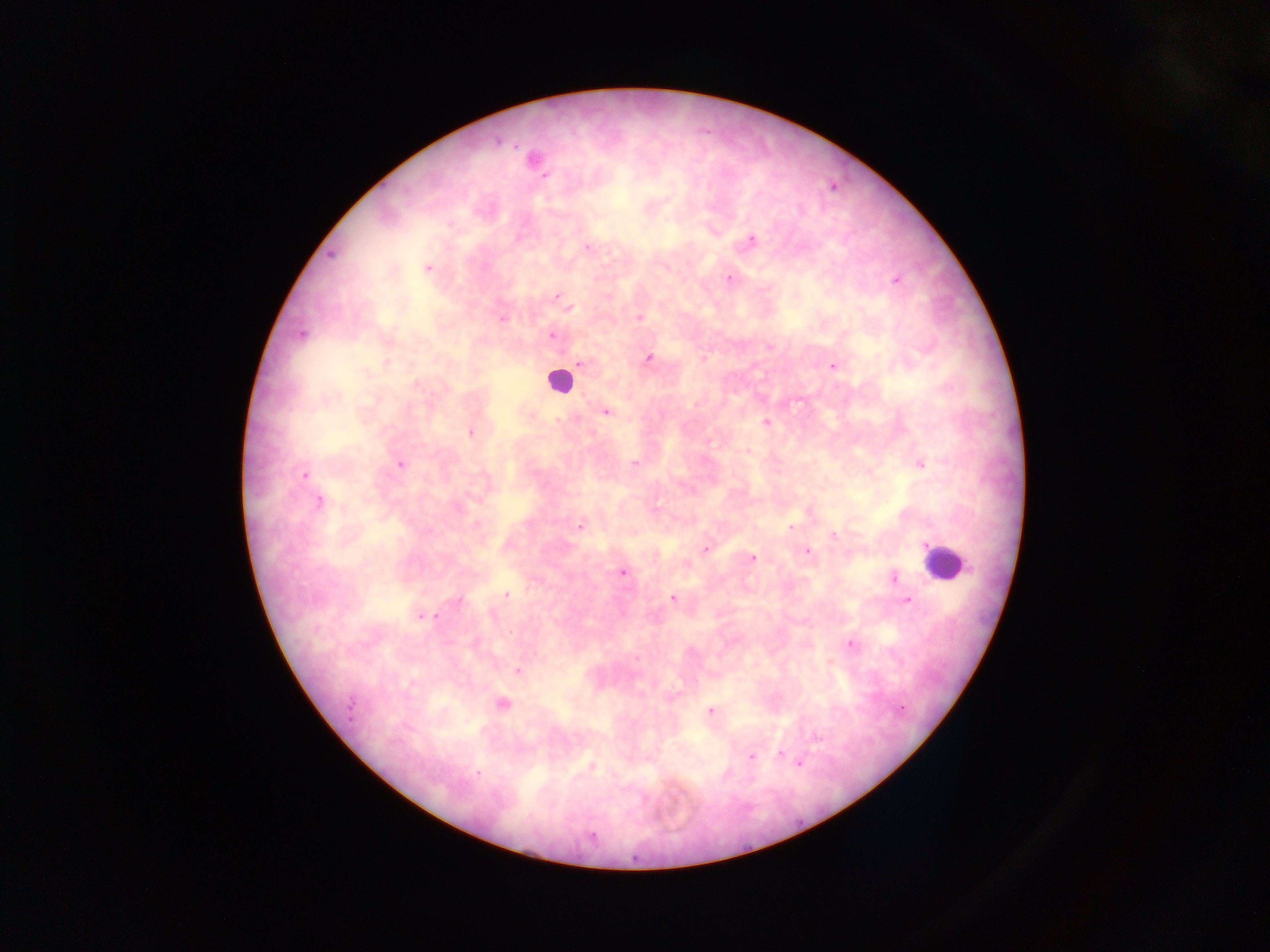

preparation: thick blood smear
country: Ghana
capture: mobile-phone photograph through a microscope
image_size: 1270×952 pixels
field_of_view: single
leukocyte_locations: 'approximate centers as [x, y] in pixels: [559, 380], [943, 562]'
malaria_parasite_locations: 'approximate centers as [x, y] in pixels: [498, 142], [534, 160], [545, 176], [752, 240], [587, 247], [427, 268], [729, 279], [896, 280], [557, 297], [563, 301], [569, 308], [638, 317], [502, 319], [302, 335], [551, 336], [648, 358], [386, 363], [581, 364], [833, 366], [606, 412], [766, 422], [470, 432], [634, 463], [921, 464], [400, 465], [305, 474], [319, 502], [580, 526], [791, 527], [834, 535], [705, 549], [807, 552], [752, 557], [623, 573], [894, 578], [507, 595], [673, 598], [458, 601], [907, 601], [435, 616], [421, 617], [510, 633], [851, 644], [518, 671], [503, 704], [350, 705], [901, 708], [710, 711], [817, 738], [780, 754], [751, 756], [799, 764], [592, 765], [478, 772], [592, 834]'